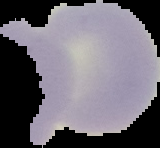
Segmented cell region on a black background. Image is 160×148 pixels. From a thin blood smear. Result: no malaria parasites detected.